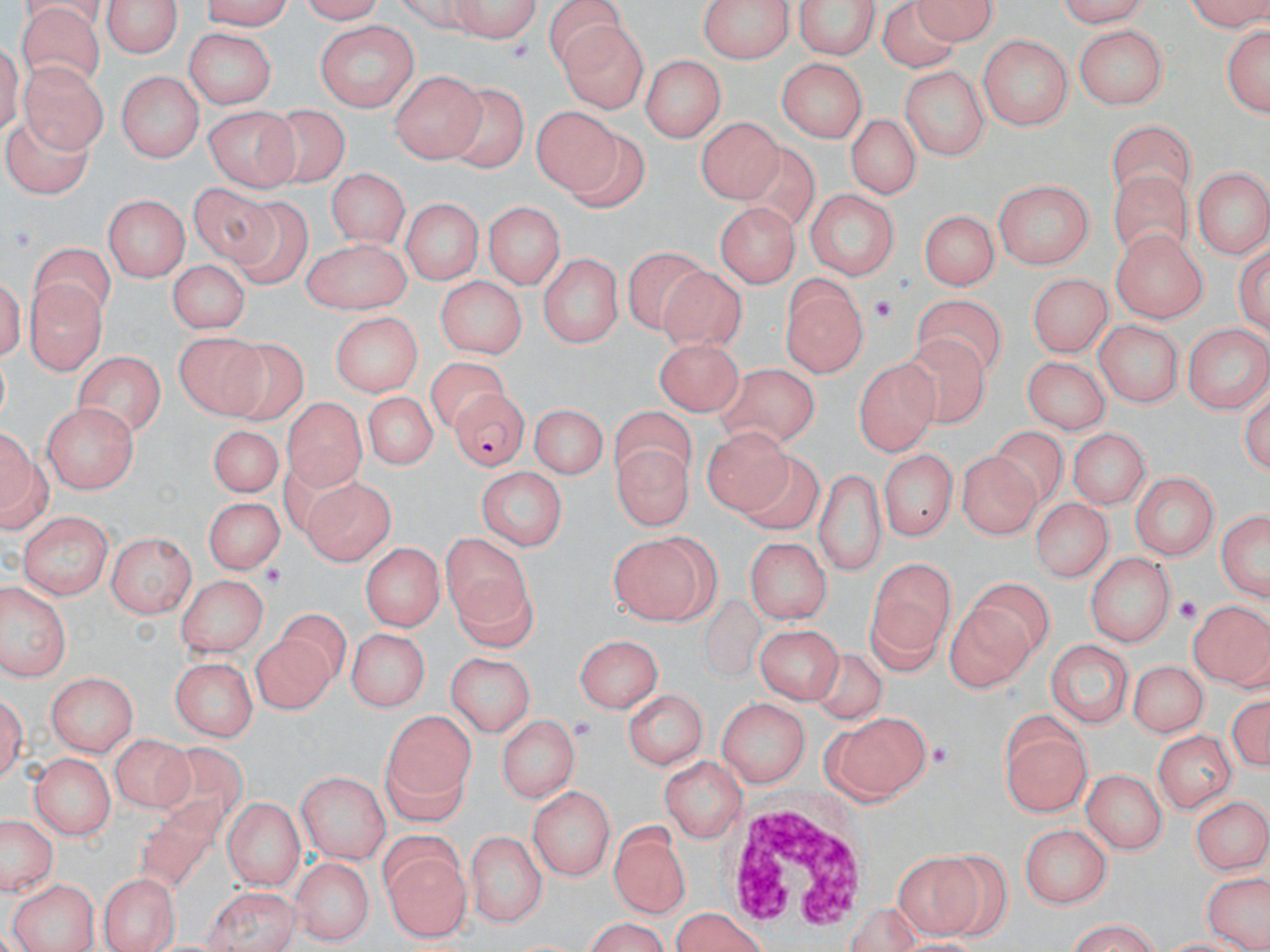
{
  "slide_level_diagnosis": "Plasmodium falciparum",
  "magnification": "1000x",
  "preparation": "thin blood film",
  "field_of_view": "single",
  "modality": "optical microscopy",
  "image_size": "1270×952 pixels",
  "uninfected_red_blood_cell_locations": "approximate bounding boxes as named x1/y1/x2/y2 corners in pixels: (x1=195, y1=0, x2=296, y2=29), (x1=291, y1=0, x2=388, y2=24), (x1=446, y1=0, x2=546, y2=40), (x1=700, y1=0, x2=792, y2=65), (x1=792, y1=0, x2=881, y2=60), (x1=1047, y1=0, x2=1159, y2=24), (x1=1183, y1=0, x2=1270, y2=34), (x1=101, y1=1, x2=184, y2=56), (x1=879, y1=2, x2=960, y2=74), (x1=913, y1=4, x2=1000, y2=49), (x1=17, y1=8, x2=107, y2=83), (x1=554, y1=19, x2=651, y2=109), (x1=317, y1=21, x2=420, y2=112), (x1=1219, y1=21, x2=1270, y2=123), (x1=1071, y1=26, x2=1164, y2=109), (x1=182, y1=29, x2=274, y2=109), (x1=977, y1=35, x2=1070, y2=129), (x1=644, y1=54, x2=724, y2=143), (x1=775, y1=57, x2=867, y2=144), (x1=19, y1=63, x2=108, y2=154), (x1=899, y1=65, x2=992, y2=158), (x1=389, y1=67, x2=485, y2=160), (x1=116, y1=71, x2=206, y2=161), (x1=448, y1=86, x2=523, y2=171), (x1=254, y1=102, x2=348, y2=180), (x1=204, y1=103, x2=301, y2=188), (x1=533, y1=107, x2=625, y2=200), (x1=8, y1=113, x2=90, y2=207), (x1=848, y1=115, x2=922, y2=199), (x1=694, y1=120, x2=780, y2=205), (x1=1111, y1=123, x2=1194, y2=200), (x1=740, y1=143, x2=821, y2=228), (x1=1111, y1=168, x2=1192, y2=264), (x1=1193, y1=168, x2=1268, y2=261), (x1=326, y1=171, x2=410, y2=247), (x1=992, y1=180, x2=1093, y2=270), (x1=189, y1=181, x2=278, y2=267), (x1=806, y1=187, x2=899, y2=283), (x1=233, y1=193, x2=312, y2=289), (x1=105, y1=194, x2=190, y2=281), (x1=401, y1=195, x2=483, y2=281), (x1=709, y1=199, x2=795, y2=285), (x1=484, y1=200, x2=567, y2=290), (x1=918, y1=209, x2=997, y2=293), (x1=1108, y1=230, x2=1207, y2=326), (x1=300, y1=237, x2=410, y2=312), (x1=32, y1=245, x2=117, y2=311), (x1=627, y1=250, x2=706, y2=329), (x1=535, y1=253, x2=625, y2=348), (x1=166, y1=259, x2=249, y2=337), (x1=657, y1=267, x2=743, y2=356), (x1=1027, y1=274, x2=1111, y2=356), (x1=435, y1=278, x2=525, y2=358), (x1=25, y1=280, x2=107, y2=378), (x1=785, y1=289, x2=864, y2=375), (x1=916, y1=299, x2=999, y2=380), (x1=329, y1=311, x2=422, y2=397), (x1=1097, y1=318, x2=1183, y2=407), (x1=1184, y1=320, x2=1269, y2=412), (x1=173, y1=336, x2=271, y2=424), (x1=652, y1=337, x2=743, y2=418), (x1=901, y1=337, x2=986, y2=426), (x1=224, y1=340, x2=306, y2=420), (x1=77, y1=349, x2=166, y2=440), (x1=1025, y1=356, x2=1111, y2=435), (x1=859, y1=359, x2=940, y2=454), (x1=432, y1=360, x2=509, y2=429), (x1=717, y1=369, x2=817, y2=447), (x1=359, y1=391, x2=439, y2=474), (x1=281, y1=396, x2=365, y2=491), (x1=533, y1=401, x2=610, y2=477), (x1=41, y1=402, x2=137, y2=491), (x1=613, y1=409, x2=693, y2=494), (x1=2, y1=422, x2=49, y2=534), (x1=205, y1=424, x2=287, y2=496), (x1=707, y1=428, x2=793, y2=517), (x1=1071, y1=429, x2=1147, y2=509), (x1=989, y1=430, x2=1069, y2=499), (x1=617, y1=443, x2=692, y2=534), (x1=879, y1=449, x2=957, y2=539), (x1=957, y1=452, x2=1039, y2=540), (x1=736, y1=453, x2=821, y2=532), (x1=814, y1=464, x2=885, y2=577), (x1=476, y1=466, x2=567, y2=548), (x1=1126, y1=473, x2=1220, y2=561), (x1=303, y1=477, x2=393, y2=564), (x1=206, y1=494, x2=284, y2=572), (x1=1029, y1=497, x2=1116, y2=579), (x1=1214, y1=507, x2=1270, y2=606), (x1=18, y1=513, x2=113, y2=598), (x1=103, y1=529, x2=199, y2=615), (x1=445, y1=533, x2=534, y2=628), (x1=744, y1=535, x2=830, y2=624), (x1=609, y1=536, x2=713, y2=621), (x1=358, y1=542, x2=447, y2=631), (x1=1086, y1=552, x2=1172, y2=647), (x1=867, y1=557, x2=957, y2=674), (x1=176, y1=574, x2=268, y2=658), (x1=968, y1=576, x2=1053, y2=659), (x1=1, y1=584, x2=74, y2=683), (x1=1187, y1=598, x2=1269, y2=691), (x1=947, y1=602, x2=1031, y2=688), (x1=279, y1=611, x2=352, y2=678), (x1=756, y1=626, x2=840, y2=706), (x1=343, y1=628, x2=432, y2=711), (x1=257, y1=634, x2=334, y2=710), (x1=579, y1=634, x2=663, y2=713), (x1=1044, y1=639, x2=1131, y2=728), (x1=815, y1=647, x2=888, y2=724), (x1=446, y1=651, x2=537, y2=736), (x1=167, y1=655, x2=260, y2=739), (x1=1126, y1=658, x2=1213, y2=737), (x1=46, y1=670, x2=139, y2=755), (x1=1, y1=681, x2=27, y2=791), (x1=622, y1=687, x2=707, y2=772), (x1=1227, y1=689, x2=1270, y2=775), (x1=718, y1=696, x2=811, y2=787), (x1=381, y1=709, x2=478, y2=824), (x1=997, y1=709, x2=1087, y2=819), (x1=499, y1=715, x2=576, y2=804), (x1=830, y1=715, x2=926, y2=804), (x1=1151, y1=730, x2=1234, y2=811), (x1=113, y1=736, x2=198, y2=809), (x1=157, y1=740, x2=247, y2=829), (x1=29, y1=753, x2=114, y2=843), (x1=659, y1=754, x2=744, y2=840), (x1=1083, y1=769, x2=1166, y2=857), (x1=296, y1=771, x2=391, y2=862), (x1=529, y1=785, x2=617, y2=881), (x1=1192, y1=792, x2=1268, y2=874), (x1=130, y1=796, x2=222, y2=900), (x1=221, y1=797, x2=305, y2=889), (x1=0, y1=814, x2=59, y2=898), (x1=612, y1=819, x2=689, y2=917), (x1=1022, y1=824, x2=1112, y2=907), (x1=466, y1=830, x2=546, y2=927), (x1=378, y1=835, x2=470, y2=941), (x1=890, y1=849, x2=984, y2=937), (x1=933, y1=853, x2=1011, y2=946), (x1=291, y1=858, x2=371, y2=946), (x1=99, y1=874, x2=179, y2=952), (x1=1206, y1=876, x2=1266, y2=950), (x1=7, y1=878, x2=97, y2=952), (x1=198, y1=886, x2=301, y2=952), (x1=669, y1=908, x2=771, y2=952), (x1=574, y1=920, x2=678, y2=950), (x1=1058, y1=925, x2=1171, y2=951)",
  "white_blood_cell_locations": "approximate bounding boxes as named x1/y1/x2/y2 corners in pixels: (x1=728, y1=800, x2=871, y2=935)",
  "platelet_locations": "approximate bounding boxes as named x1/y1/x2/y2 corners in pixels: (x1=870, y1=294, x2=899, y2=328), (x1=263, y1=565, x2=285, y2=589), (x1=1175, y1=592, x2=1205, y2=626), (x1=572, y1=714, x2=592, y2=740), (x1=926, y1=741, x2=955, y2=772)",
  "plasmodium_falciparum_infected_red_blood_cell_locations": "approximate bounding boxes as named x1/y1/x2/y2 corners in pixels: (x1=453, y1=392, x2=530, y2=471)",
  "stain": "May-Grünwald-Giemsa"
}